Identify the parasite.
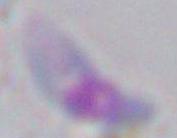
This is Toxoplasma gondii.

Summary:
  - Magnification: 1000x
  - Modality: photomicrograph